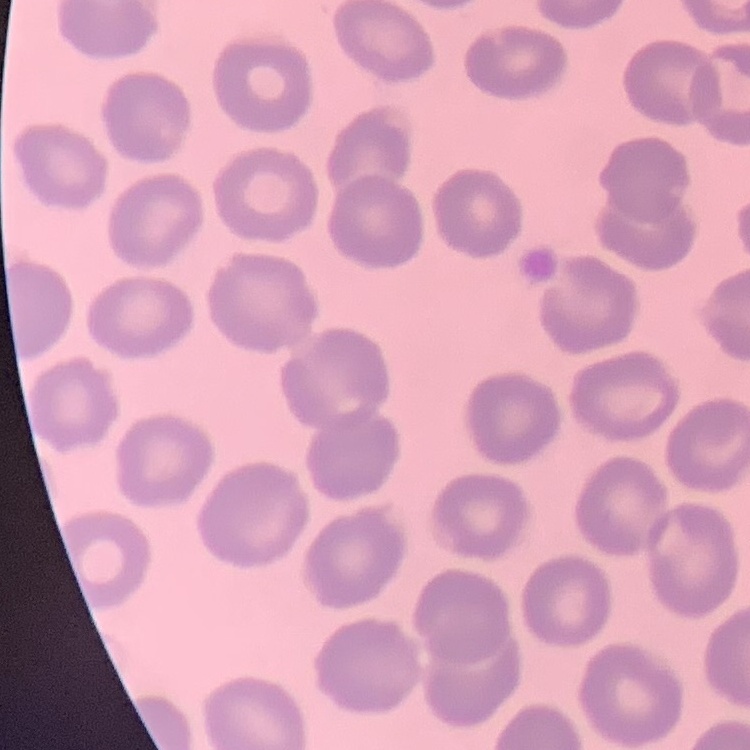

erythrocyte morphology = no rouleaux formation
stain = Field's or Giemsa
image type = square crop of a larger photomicrograph
preparation = thin peripheral smear